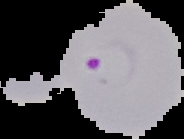
Image is 184×139 pixels. From a thin blood smear. Malaria status: parasitized. Cell region segmented out of the field of view; the surrounding area is masked to black.